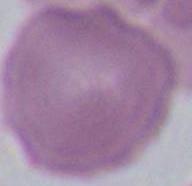
An erythrocyte is shown. Captured at 1000x magnification. Photomicrograph.